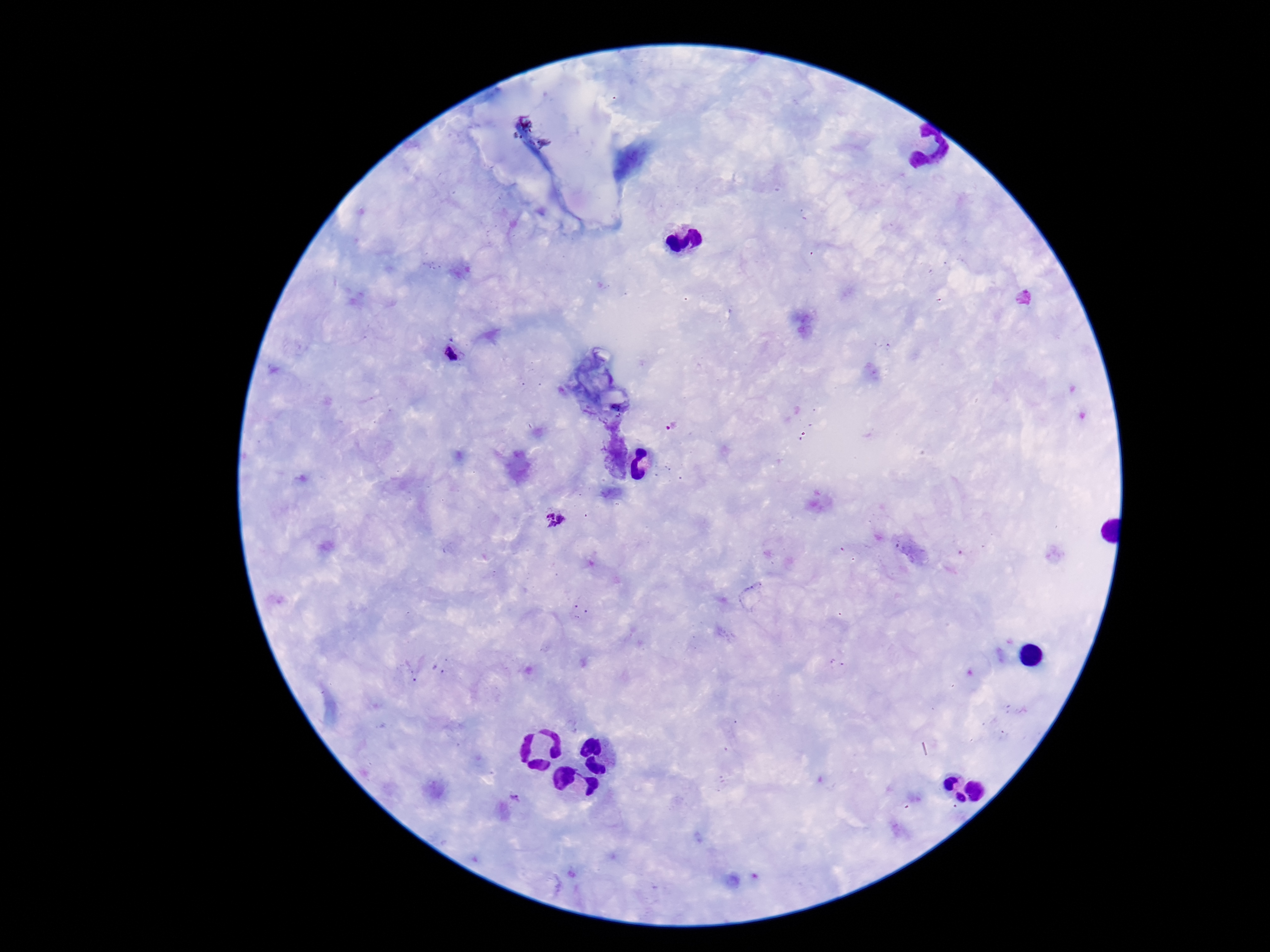

Approximate centers as [x, y] in pixels. Plasmodium parasite locations: [453, 353], [672, 426], [552, 516], [514, 798]. Giemsa stain. One field from this slide. Image is 1270×952 pixels. 100x magnification. Thick peripheral-blood smear. Patient malaria status: positive. Smartphone photograph taken through the microscope eyepiece.